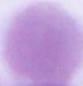

Summary:
  - Magnification: 1000x
  - Identification: erythrocyte
  - Modality: photomicrograph